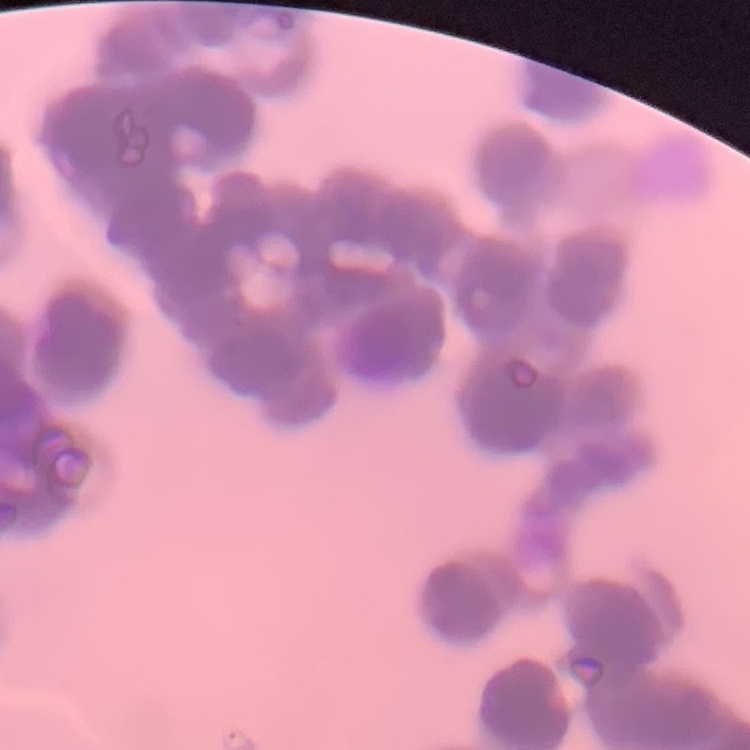

{
  "erythrocyte_morphology": "rouleaux formation",
  "image_type": "square crop of a larger photomicrograph",
  "stain": "Field's or Giemsa",
  "preparation": "thin peripheral smear"
}